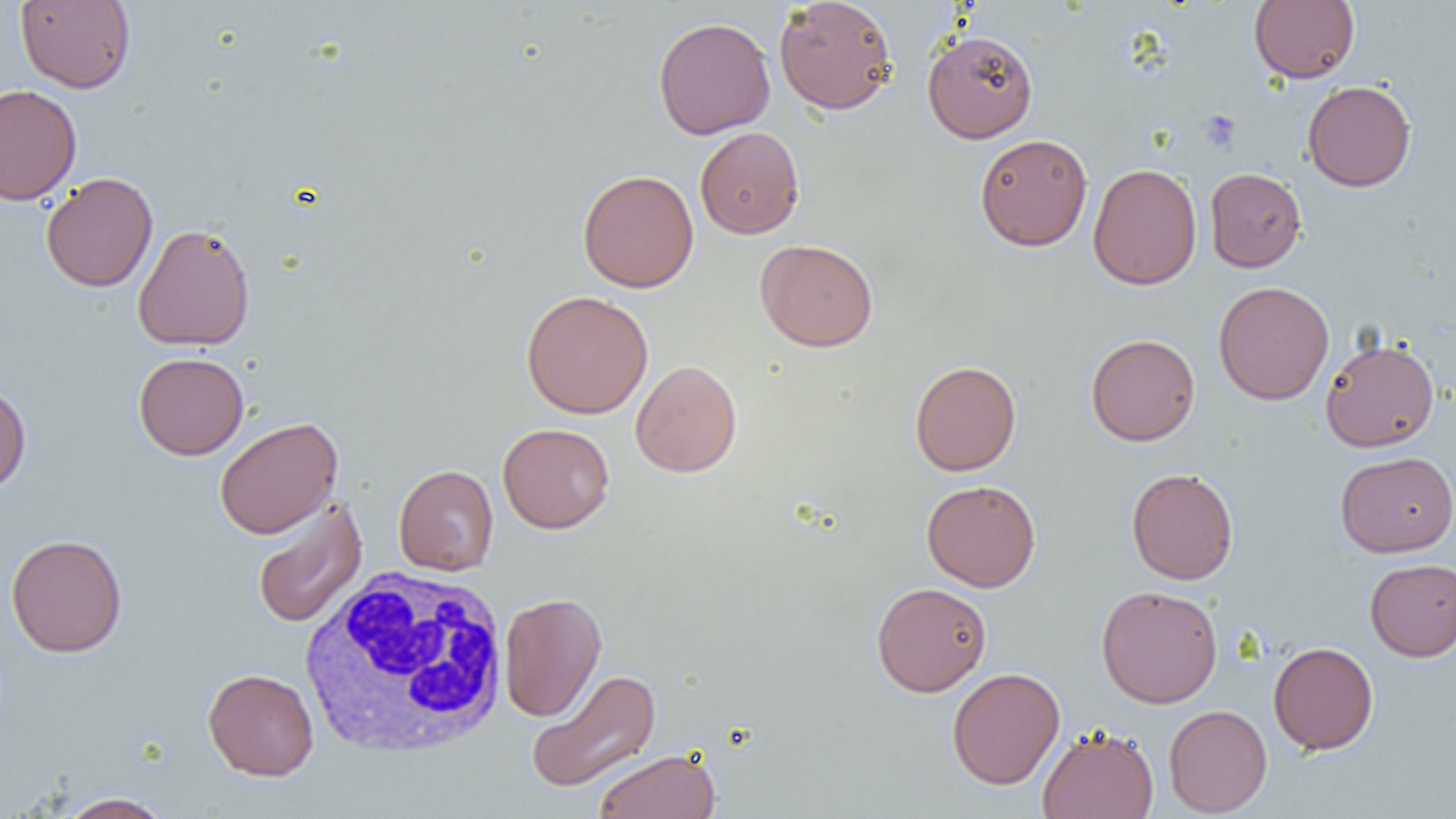

slide_level_diagnosis: no evidence of blood parasites
preparation: thin blood smear
uninfected_red_blood_cell_locations: 'approximate bounding boxes as (x1,y1)-(x2,y2) corner pairs in pixels: (15,0)-(136,92), (774,0)-(898,115), (1249,1)-(1360,83), (653,16)-(776,140), (922,29)-(1038,143), (1302,80)-(1416,192), (0,84)-(82,205), (695,126)-(804,239), (974,133)-(1093,251), (1087,163)-(1202,290), (1204,167)-(1307,272), (577,169)-(699,292), (40,172)-(158,293), (132,223)-(255,351), (755,239)-(878,352), (1213,281)-(1334,405), (521,290)-(653,419), (1085,333)-(1201,445), (1320,338)-(1439,452), (133,352)-(249,460), (630,360)-(742,477), (909,360)-(1021,476), (0,383)-(32,494), (214,417)-(343,539), (498,423)-(615,534), (1335,451)-(1456,557), (393,464)-(499,576), (1126,467)-(1239,584), (922,479)-(1040,592), (251,497)-(367,630), (5,533)-(128,657), (1365,558)-(1456,661), (871,581)-(991,696), (1096,585)-(1223,708), (499,592)-(607,722), (1268,641)-(1379,754), (947,667)-(1065,790), (203,668)-(319,780), (525,669)-(661,793), (1163,704)-(1272,817), (1037,725)-(1159,819), (594,748)-(721,819), (57,792)-(172,819)'
magnification: 1000x
field_of_view: one of a larger specimen
image_size: 1456×819 pixels
white_blood_cell_locations: 'approximate bounding boxes as (x1,y1)-(x2,y2) corner pairs in pixels: (300,563)-(512,759)'
platelet_locations: 'approximate bounding boxes as (x1,y1)-(x2,y2) corner pairs in pixels: (1198,110)-(1242,152)'
modality: optical microscopy